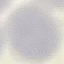

Summary:
  - Result: no malaria parasites seen
  - Image type: cell patch, automatically extracted from a larger field of view and resized to 64 × 64 pixels
  - Preparation: thin blood film
  - Stain: Giemsa
  - Capture: smartphone camera at the microscope eyepiece